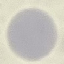
Summary:
  - Result: no malaria parasites seen
  - Image type: automatically extracted cell patch, resized to 64 × 64 pixels
  - Stain: Giemsa
  - Preparation: thin blood smear
  - Capture: smartphone camera at the microscope eyepiece